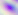

modality = photomicrograph
magnification = 400x
identification = Toxoplasma gondii